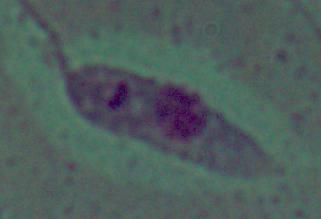
Summary:
  - Identification: Leishmania
  - Magnification: 1000x
  - Modality: micrograph